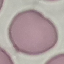
Summary:
  - Malaria status: uninfected
  - Capture: smartphone camera at the microscope eyepiece
  - Stain: Giemsa
  - Image type: cell patch, automatically extracted from a larger field of view and resized to 64 × 64 pixels
  - Preparation: thin blood film